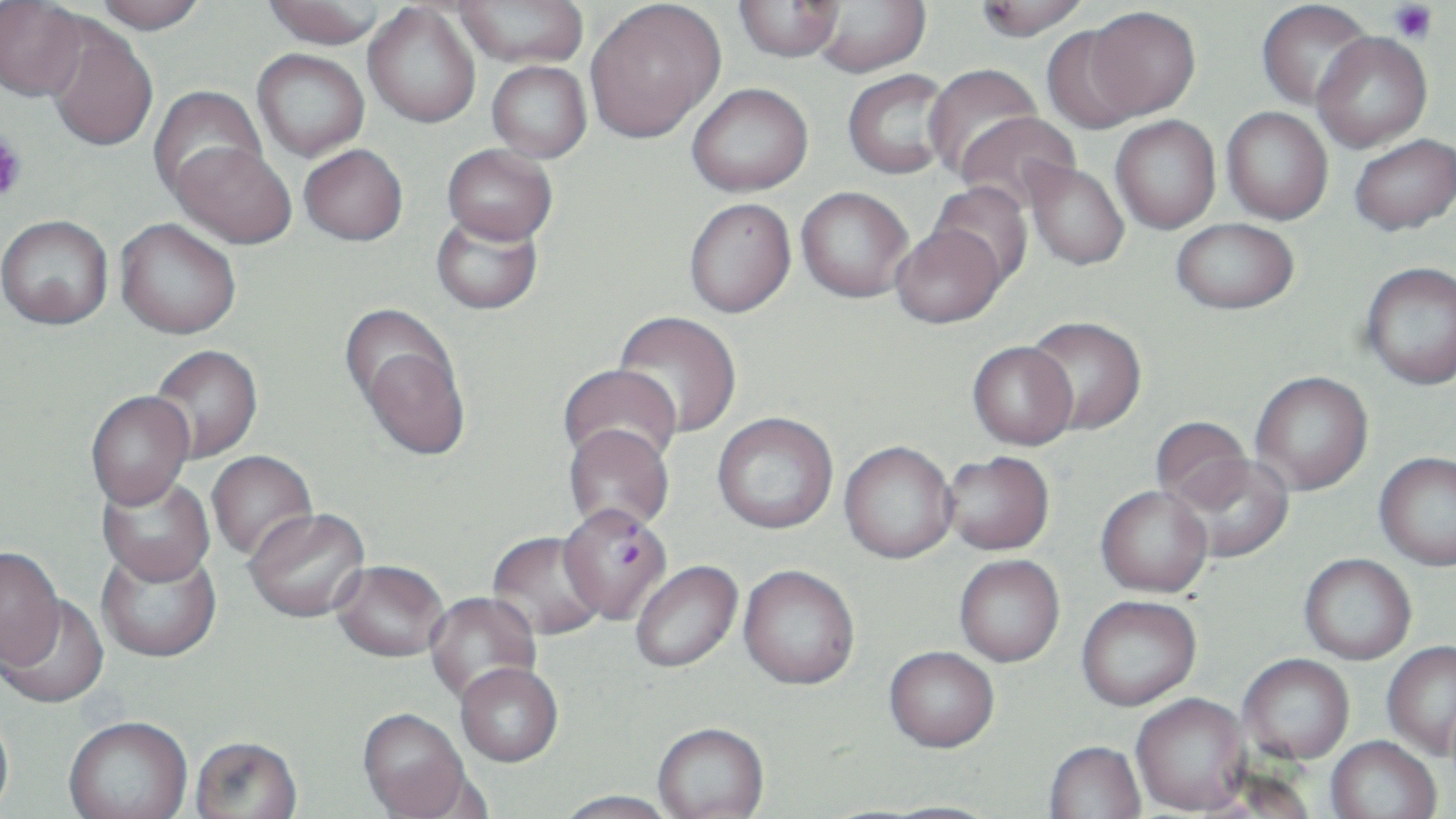

Summary:
  - Coordinate format: approximate bounding boxes as named x1/y1/x2/y2 corners in pixels
  - Uninfected red blood cell locations: (x1=92, y1=0, x2=207, y2=34), (x1=261, y1=0, x2=388, y2=48), (x1=453, y1=0, x2=588, y2=68), (x1=974, y1=0, x2=1089, y2=40), (x1=1256, y1=0, x2=1375, y2=112), (x1=585, y1=1, x2=725, y2=144), (x1=733, y1=1, x2=845, y2=61), (x1=809, y1=1, x2=931, y2=77), (x1=0, y1=2, x2=88, y2=102), (x1=363, y1=4, x2=481, y2=128), (x1=1085, y1=6, x2=1201, y2=121), (x1=44, y1=21, x2=158, y2=152), (x1=1039, y1=24, x2=1150, y2=134), (x1=1312, y1=32, x2=1432, y2=152), (x1=252, y1=49, x2=369, y2=161), (x1=487, y1=61, x2=592, y2=163), (x1=923, y1=63, x2=1047, y2=180), (x1=843, y1=69, x2=954, y2=179), (x1=687, y1=83, x2=813, y2=196), (x1=149, y1=85, x2=267, y2=200), (x1=1221, y1=107, x2=1333, y2=224), (x1=955, y1=111, x2=1081, y2=214), (x1=1111, y1=116, x2=1221, y2=234), (x1=1349, y1=134, x2=1456, y2=235), (x1=168, y1=141, x2=297, y2=249), (x1=299, y1=144, x2=408, y2=246), (x1=442, y1=144, x2=558, y2=245), (x1=1026, y1=163, x2=1129, y2=270), (x1=928, y1=181, x2=1035, y2=287), (x1=796, y1=187, x2=914, y2=302), (x1=684, y1=199, x2=796, y2=317), (x1=430, y1=209, x2=544, y2=315), (x1=0, y1=215, x2=113, y2=329), (x1=115, y1=218, x2=240, y2=340), (x1=1171, y1=218, x2=1298, y2=314), (x1=892, y1=224, x2=1004, y2=328), (x1=1361, y1=261, x2=1456, y2=390), (x1=613, y1=310, x2=742, y2=439), (x1=345, y1=311, x2=470, y2=463), (x1=1025, y1=316, x2=1146, y2=435), (x1=967, y1=341, x2=1077, y2=450), (x1=148, y1=345, x2=263, y2=464), (x1=558, y1=364, x2=681, y2=472), (x1=1250, y1=371, x2=1373, y2=495), (x1=86, y1=393, x2=194, y2=514), (x1=712, y1=414, x2=838, y2=535), (x1=1150, y1=416, x2=1253, y2=513), (x1=563, y1=426, x2=674, y2=536), (x1=839, y1=443, x2=958, y2=566), (x1=206, y1=452, x2=317, y2=564), (x1=943, y1=452, x2=1055, y2=556), (x1=1374, y1=452, x2=1456, y2=572), (x1=1174, y1=454, x2=1295, y2=563), (x1=96, y1=475, x2=216, y2=591), (x1=1096, y1=485, x2=1213, y2=597), (x1=245, y1=510, x2=372, y2=625), (x1=487, y1=533, x2=606, y2=644), (x1=96, y1=548, x2=222, y2=665), (x1=0, y1=549, x2=66, y2=674), (x1=1299, y1=553, x2=1416, y2=664), (x1=955, y1=555, x2=1065, y2=667), (x1=631, y1=562, x2=743, y2=675), (x1=331, y1=564, x2=448, y2=665), (x1=738, y1=568, x2=860, y2=693), (x1=424, y1=592, x2=542, y2=708), (x1=1, y1=595, x2=110, y2=711), (x1=1076, y1=595, x2=1202, y2=710), (x1=1382, y1=641, x2=1456, y2=760), (x1=883, y1=649, x2=999, y2=755), (x1=1239, y1=654, x2=1354, y2=764), (x1=456, y1=667, x2=563, y2=769), (x1=1131, y1=694, x2=1251, y2=816), (x1=0, y1=709, x2=15, y2=819), (x1=357, y1=711, x2=473, y2=819), (x1=63, y1=720, x2=193, y2=819), (x1=653, y1=725, x2=769, y2=819), (x1=1325, y1=736, x2=1441, y2=819), (x1=189, y1=739, x2=304, y2=819), (x1=1044, y1=741, x2=1146, y2=819), (x1=553, y1=792, x2=680, y2=819), (x1=876, y1=801, x2=1003, y2=819)
  - Plasmodium falciparum-infected red blood cell locations: (x1=558, y1=507, x2=670, y2=626)
  - Platelet locations: (x1=1390, y1=2, x2=1437, y2=44), (x1=0, y1=130, x2=28, y2=204)
  - Slide-level diagnosis: Plasmodium falciparum
  - Magnification: 1000x
  - Image size: 1456×819 pixels
  - Field of view: single
  - Modality: light microscopy
  - Stain: May-Grünwald-Giemsa
  - Preparation: thin blood smear